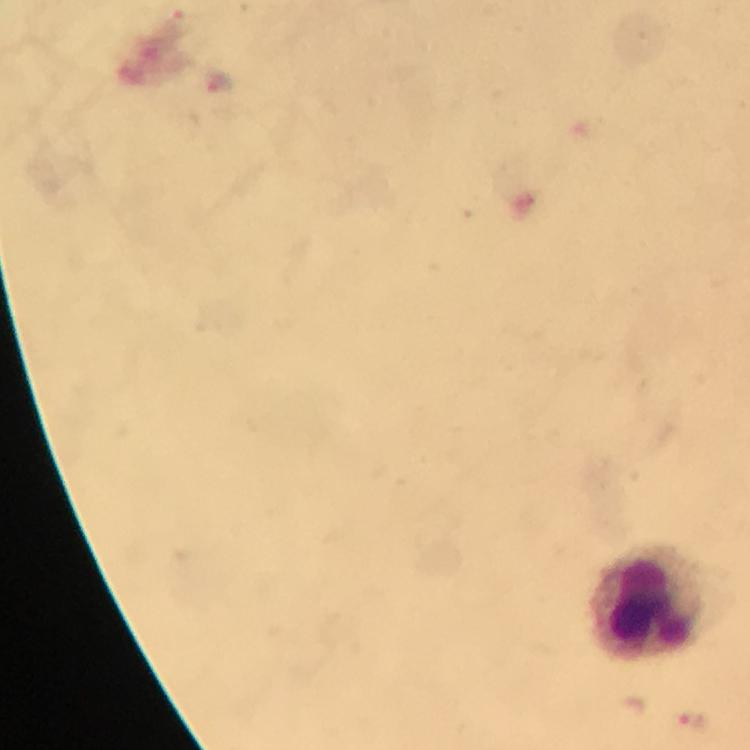

image size = 750×750 pixels
capture = smartphone mounted on the microscope
magnification = 100x
immersion oil = applied
preparation = thick blood film
stain = Giemsa
cropped from = a single field of view
context = from a diagnostic examination for malaria
Plasmodium parasite locations = approximate centers as [x, y] in pixels: [218, 83], [693, 722]
leukocyte locations = approximate centers as [x, y] in pixels: [648, 603]